Outline each uninfected red blood cell.
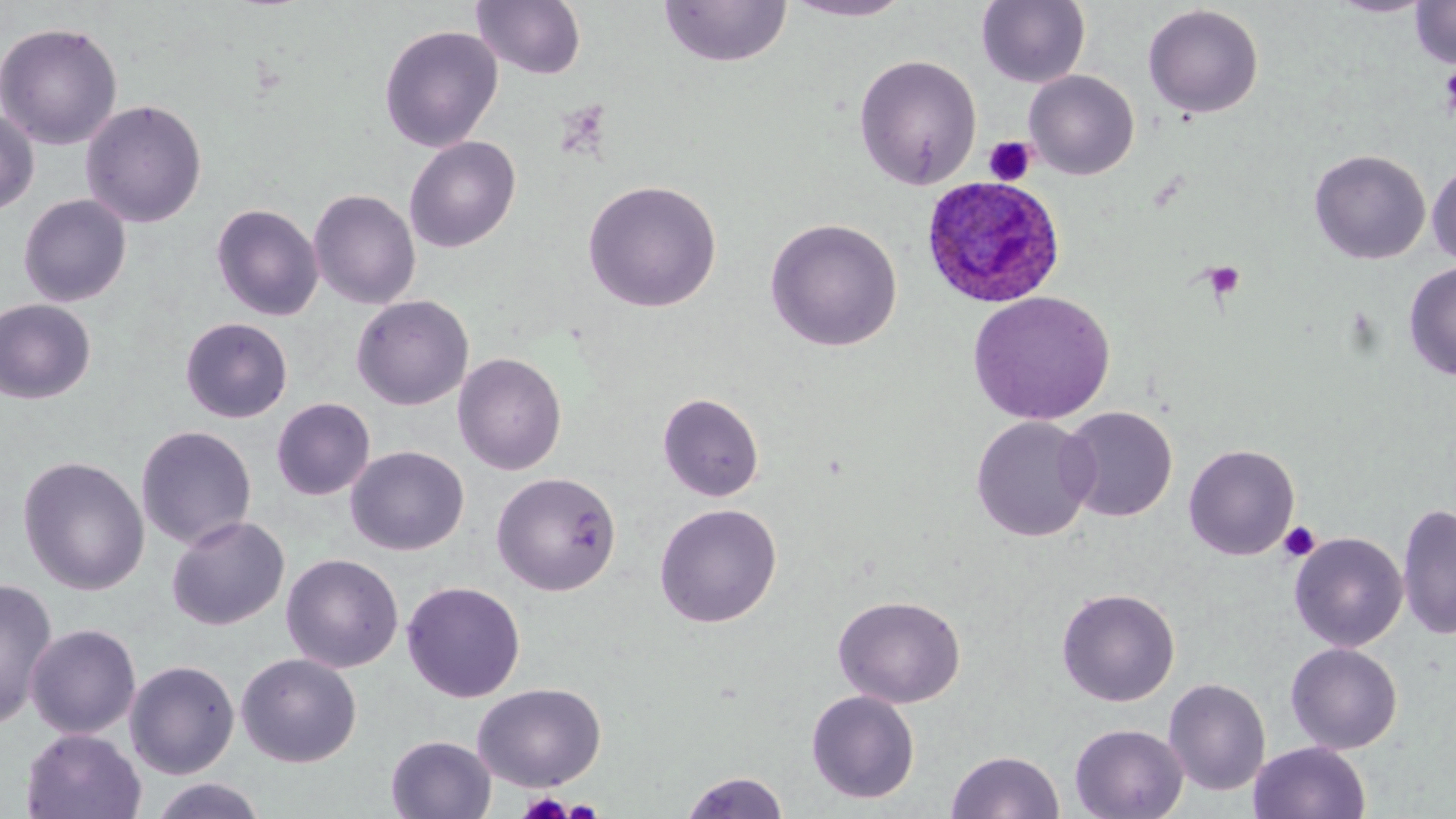
Approximate bounding boxes as named x1/y1/x2/y2 corners in pixels.
Uninfected red blood cells: (x1=783, y1=0, x2=915, y2=22), (x1=976, y1=0, x2=1091, y2=88), (x1=1329, y1=0, x2=1434, y2=17), (x1=472, y1=1, x2=587, y2=80), (x1=659, y1=1, x2=792, y2=68), (x1=1410, y1=1, x2=1456, y2=68), (x1=1142, y1=4, x2=1264, y2=118), (x1=0, y1=21, x2=123, y2=150), (x1=378, y1=24, x2=503, y2=152), (x1=853, y1=54, x2=982, y2=189), (x1=1024, y1=70, x2=1139, y2=180), (x1=80, y1=99, x2=207, y2=228), (x1=0, y1=109, x2=39, y2=216), (x1=404, y1=135, x2=522, y2=253), (x1=1309, y1=149, x2=1431, y2=265), (x1=1427, y1=160, x2=1456, y2=266), (x1=583, y1=179, x2=722, y2=312), (x1=308, y1=188, x2=421, y2=310), (x1=18, y1=194, x2=132, y2=308), (x1=211, y1=203, x2=324, y2=321), (x1=764, y1=217, x2=903, y2=351), (x1=1403, y1=262, x2=1456, y2=380), (x1=967, y1=291, x2=1116, y2=426), (x1=351, y1=295, x2=474, y2=411), (x1=0, y1=299, x2=97, y2=404), (x1=180, y1=317, x2=293, y2=423), (x1=452, y1=352, x2=567, y2=475), (x1=658, y1=393, x2=764, y2=502), (x1=271, y1=398, x2=375, y2=501), (x1=1058, y1=406, x2=1178, y2=522), (x1=969, y1=415, x2=1099, y2=542), (x1=136, y1=425, x2=257, y2=549), (x1=1184, y1=444, x2=1300, y2=560), (x1=345, y1=445, x2=469, y2=556), (x1=17, y1=456, x2=150, y2=595), (x1=491, y1=471, x2=622, y2=596), (x1=654, y1=502, x2=782, y2=628), (x1=1397, y1=502, x2=1456, y2=641), (x1=166, y1=515, x2=290, y2=631), (x1=1289, y1=532, x2=1408, y2=651), (x1=281, y1=553, x2=403, y2=673), (x1=0, y1=577, x2=59, y2=730), (x1=401, y1=580, x2=526, y2=703), (x1=1056, y1=587, x2=1180, y2=706), (x1=833, y1=594, x2=966, y2=708), (x1=25, y1=623, x2=141, y2=739), (x1=1285, y1=642, x2=1403, y2=754), (x1=236, y1=652, x2=362, y2=767), (x1=125, y1=660, x2=240, y2=779), (x1=1163, y1=677, x2=1270, y2=796), (x1=472, y1=682, x2=607, y2=791), (x1=805, y1=690, x2=920, y2=804), (x1=1070, y1=723, x2=1189, y2=819), (x1=21, y1=728, x2=146, y2=818), (x1=385, y1=734, x2=496, y2=819), (x1=1249, y1=741, x2=1371, y2=819), (x1=946, y1=750, x2=1064, y2=819), (x1=679, y1=770, x2=789, y2=818), (x1=148, y1=778, x2=267, y2=818).

Platelet locations: (x1=1440, y1=62, x2=1456, y2=119), (x1=983, y1=136, x2=1037, y2=186), (x1=1201, y1=261, x2=1245, y2=300), (x1=1279, y1=521, x2=1321, y2=562), (x1=518, y1=791, x2=573, y2=818), (x1=562, y1=799, x2=604, y2=818). Plasmodium ovale-infected red blood cell locations: (x1=921, y1=175, x2=1065, y2=308). Slide-level diagnosis: Plasmodium ovale. Optical microscopy. 1000x magnification. May-Grünwald-Giemsa stain. Image is 1456×819 pixels. Single field of view. Thin blood smear.